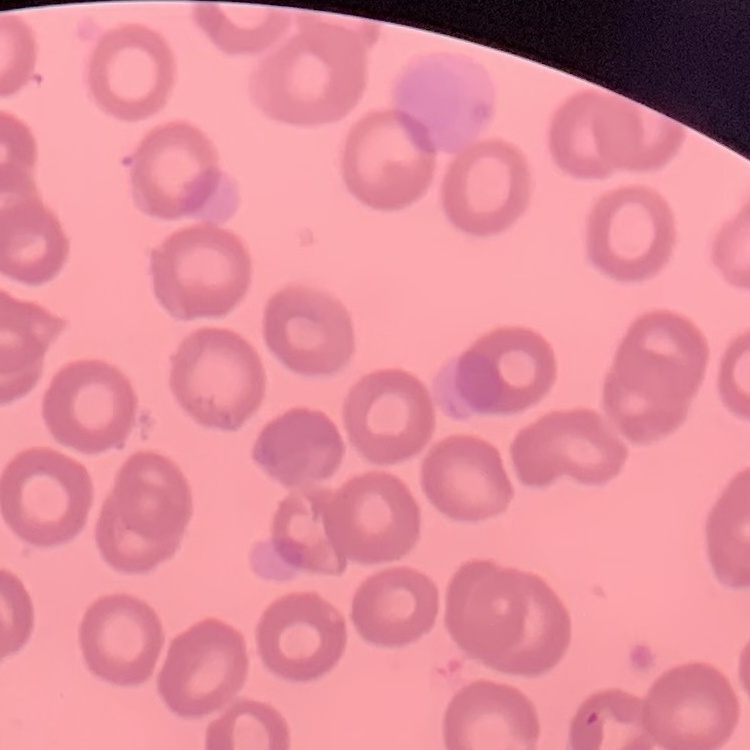 The red blood cells show no rouleaux formation. Thin blood film. Square crop of a larger photomicrograph. Field's or Giemsa stain.